Name the parasite shown.
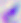

Toxoplasma gondii.

Micrograph. Captured at 400x magnification.